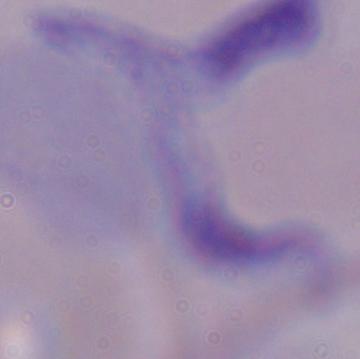

modality: photomicrograph
identification: trypanosome
magnification: 1000x